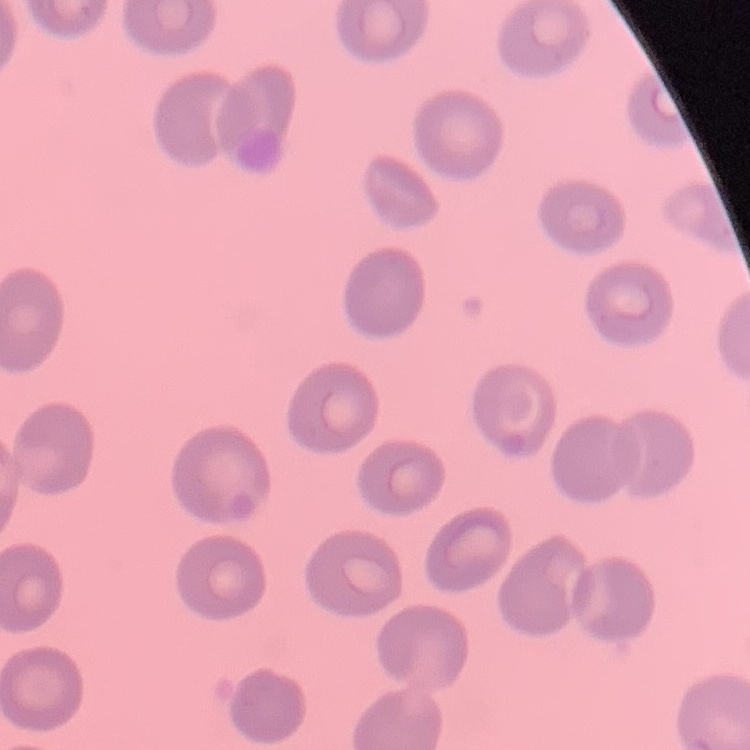 The erythrocytes exhibit no rouleaux formation. One tile cut from a larger photomicrograph. Field's or Giemsa stain. Thin blood smear.